Classify this cell by malaria status.
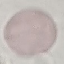
It is uninfected.

Summary:
  - Capture: smartphone through the microscope eyepiece
  - Stain: Giemsa
  - Preparation: thin smear
  - Image type: cell patch, automatically extracted from a larger field of view and resized to 64 × 64 pixels